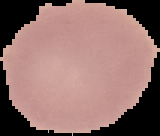 The area outside the segmented cell region is set to black. From a thin blood smear. Image is 160×136 pixels. Malaria status: uninfected.